Classify this cell by malaria status.
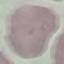

Uninfected.

Thin blood film. Acquired by smartphone through the microscope eyepiece. Giemsa-stained preparation. Cell patch, automatically extracted from a larger field of view and resized to 64 × 64 pixels.